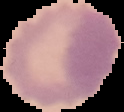 Result: no malaria parasites detected. From a thin blood film. The area outside the segmented cell region is set to black. Image is 124×112 pixels.